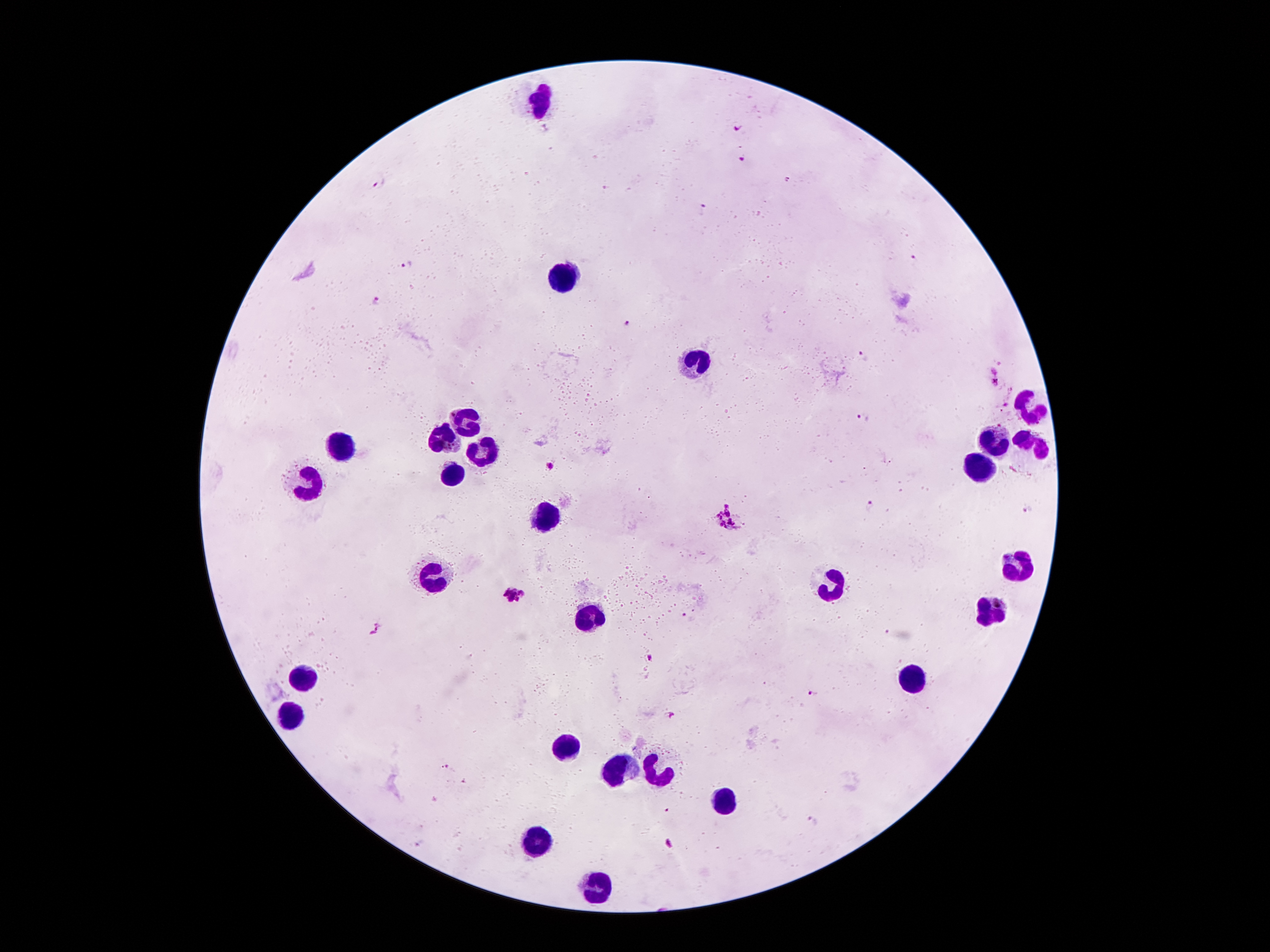 Approximate object centers, in pixels from the top-left corner. Plasmodium parasite locations: (x=735, y=125), (x=741, y=156), (x=381, y=183), (x=702, y=209), (x=408, y=264), (x=373, y=302), (x=628, y=321), (x=863, y=357), (x=995, y=377), (x=862, y=419), (x=550, y=466), (x=870, y=506), (x=1027, y=509), (x=727, y=517), (x=514, y=594), (x=376, y=630), (x=649, y=656), (x=812, y=692), (x=670, y=713), (x=444, y=767), (x=812, y=823), (x=420, y=843). Leukocyte locations: (x=542, y=102), (x=565, y=274), (x=700, y=360), (x=1030, y=407), (x=467, y=419), (x=444, y=438), (x=991, y=442), (x=337, y=446), (x=1032, y=448), (x=483, y=452), (x=975, y=466), (x=452, y=472), (x=311, y=481), (x=544, y=522), (x=1018, y=566), (x=436, y=573), (x=826, y=582), (x=992, y=615), (x=593, y=617), (x=303, y=671), (x=908, y=676), (x=289, y=715), (x=567, y=743), (x=621, y=769), (x=658, y=771), (x=721, y=797), (x=534, y=839), (x=600, y=888). Patient malaria status: infected with Plasmodium falciparum. Giemsa-stained preparation. One field from this slide. 100x magnification. Thick blood film. Image is 1270×952 pixels. Smartphone photograph taken through the microscope eyepiece.